Point out each Plasmodium parasite and each leukocyte.
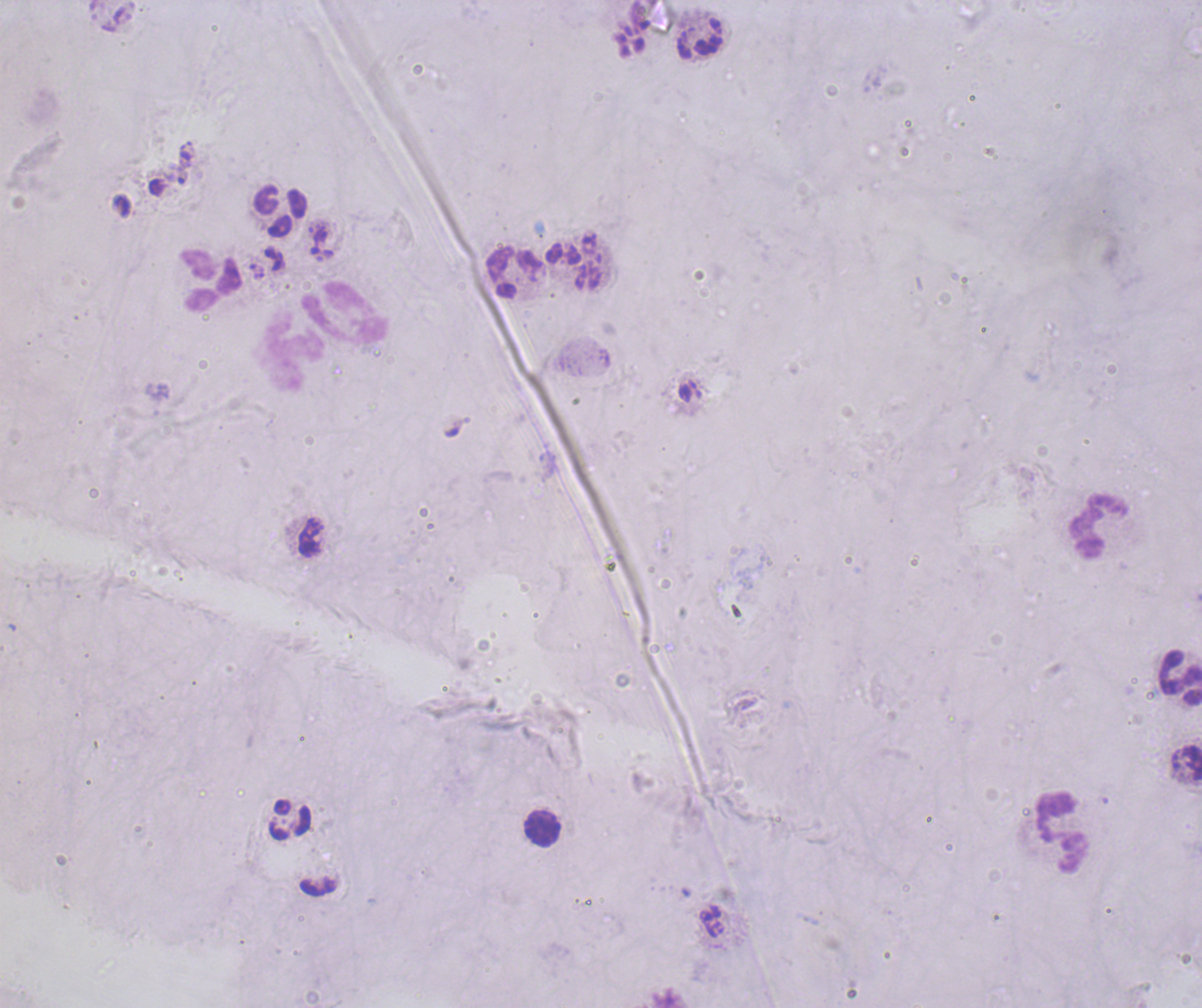
Negative for Plasmodium parasites.
Approximate centers as (x, y) in pixels.
Leukocytes: (280, 212), (514, 271), (209, 279), (344, 314), (294, 352), (1098, 527), (1180, 677), (289, 820), (542, 827), (1061, 830).

Summary:
  - Field of view: one from this slide
  - Preparation: thick blood smear
  - Context: previously used in a real diagnosis
  - Coloration quality: bad
  - Stain: Romanowsky
  - Image size: 1202×1008 pixels
  - Background quality: poor
  - Magnification: 100x